Locate every Plasmodium parasite and every leukocyte.
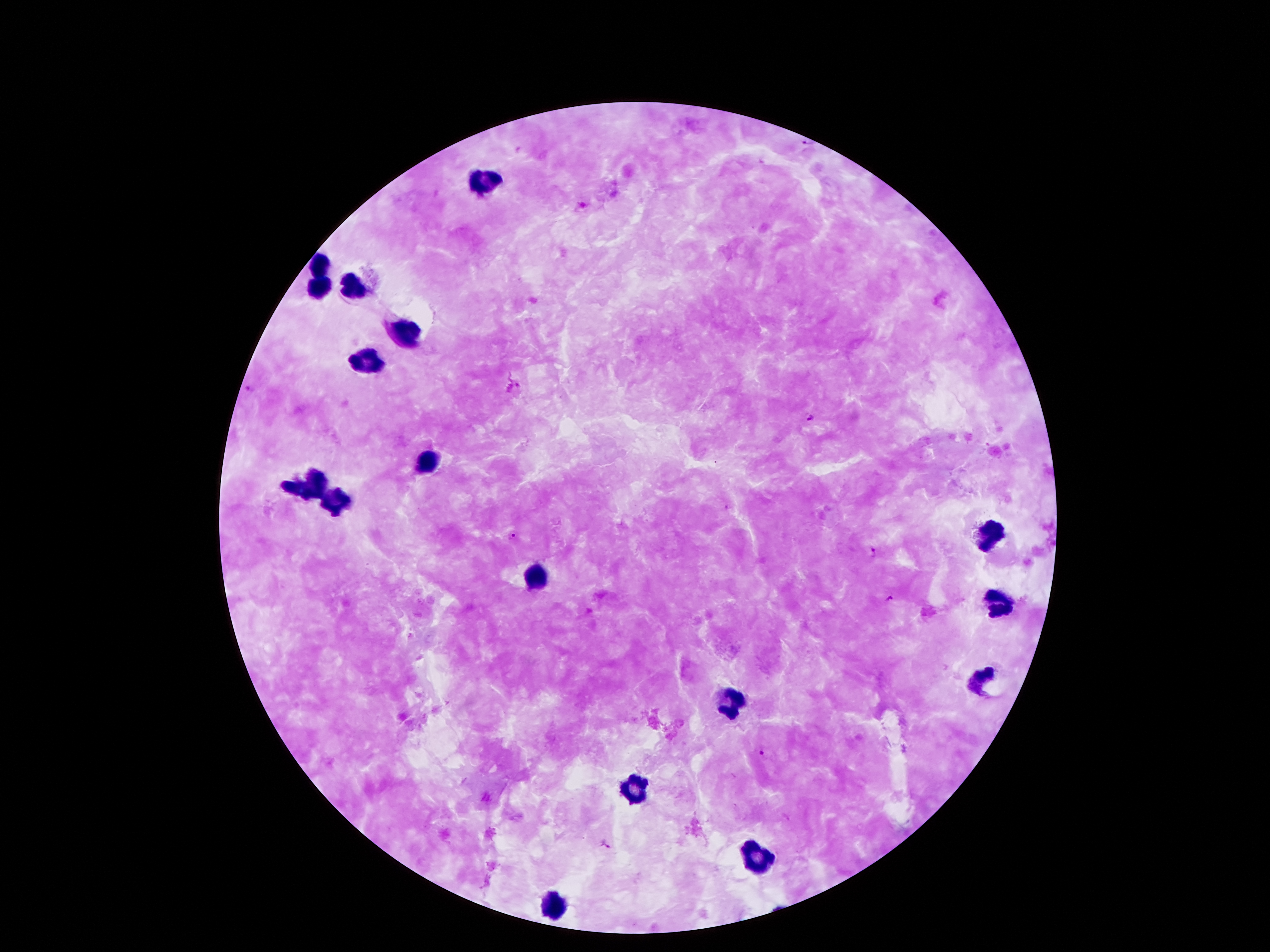
Approximate centers as {x, y} in pixels.
Plasmodium parasites: {808, 140}, {249, 389}, {808, 417}, {515, 535}, {872, 552}, {891, 598}, {762, 753}, {605, 845}.
Leukocytes: {484, 175}, {318, 264}, {318, 286}, {355, 290}, {407, 325}, {372, 362}, {429, 459}, {324, 479}, {296, 490}, {340, 502}, {990, 535}, {536, 575}, {998, 604}, {978, 676}, {726, 706}, {639, 789}, {756, 857}, {555, 904}.

stain = Giemsa
capture = smartphone through the microscope eyepiece
image size = 1270×952 pixels
preparation = thick blood smear
patient malaria status = positive for Plasmodium falciparum
field of view = one from this slide
magnification = 100x